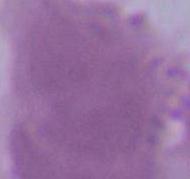

An erythrocyte is shown. Micrograph. Captured at 1000x magnification.